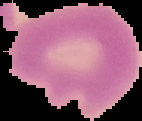 Malaria status: uninfected. From a thin blood film. The area outside the segmented cell region is set to black. Image is 142×121 pixels.